Name the parasite shown.
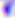
This is Toxoplasma gondii.

modality = photomicrograph
magnification = 400x